Report the malaria status of this cell.
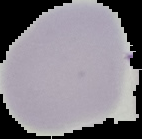

Uninfected.

The area outside the segmented cell region is set to black. From a thin blood film. Image is 142×139 pixels.